Locate and identify every blood parasite.
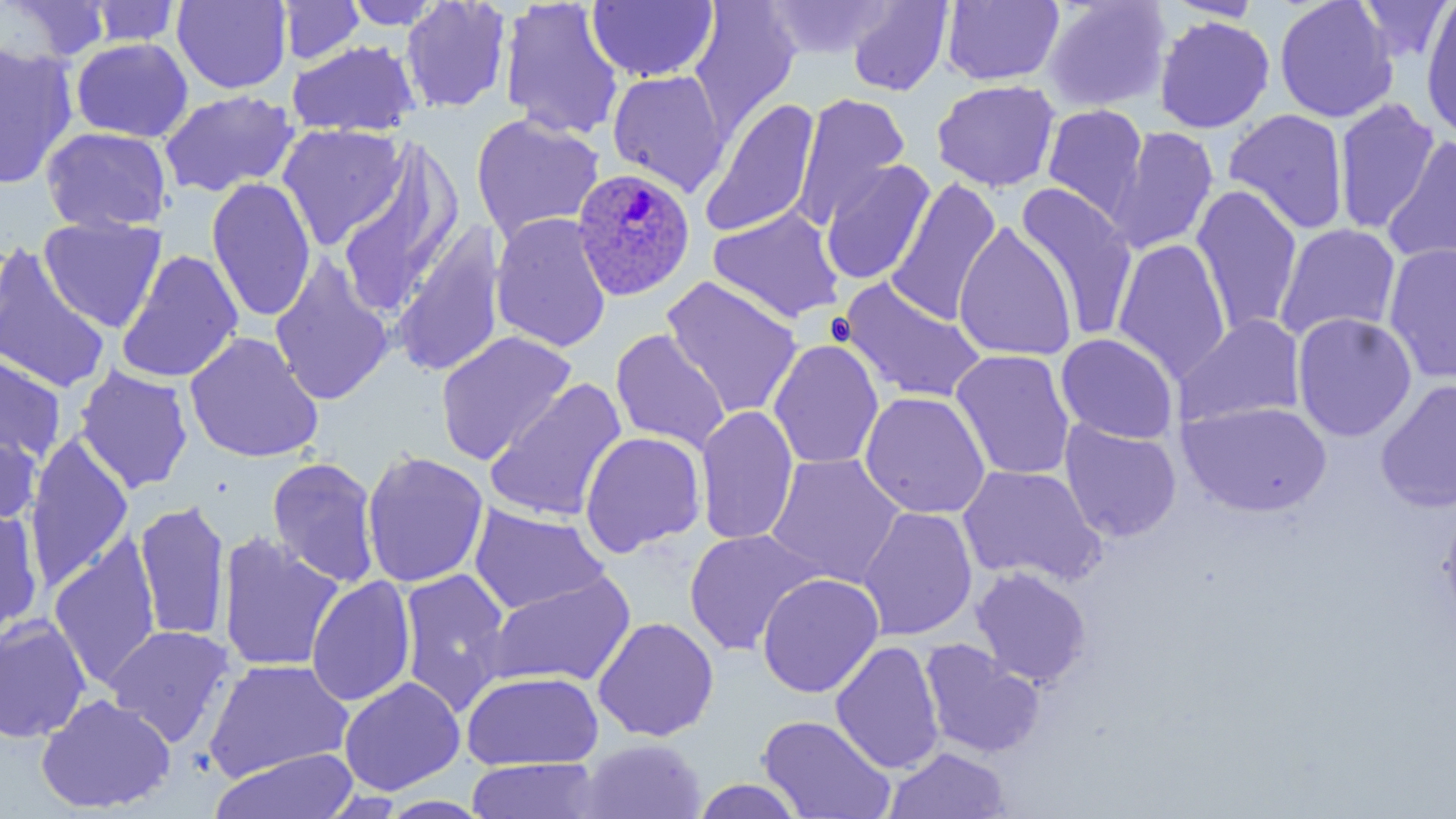

Approximate bounding boxes as [x1, y1, x2, y2] in pixels.
Plasmodium ovale-infected red blood cells: [572, 167, 695, 302].
No Plasmodium falciparum, Plasmodium malariae, Plasmodium vivax, Babesia divergens, or Trypanosoma brucei observed.

slide-level diagnosis = Plasmodium ovale
uninfected red blood cell locations = approximate bounding boxes as [x1, y1, x2, y2] in pixels: [2, 0, 112, 63], [498, 0, 624, 140], [586, 0, 719, 83], [941, 0, 1064, 86], [1041, 0, 1173, 113], [1355, 0, 1453, 62], [84, 1, 183, 47], [171, 1, 292, 94], [277, 1, 366, 65], [340, 1, 446, 30], [400, 1, 512, 114], [688, 1, 801, 137], [760, 1, 896, 61], [846, 1, 952, 96], [1273, 1, 1399, 123], [1420, 1, 1456, 141], [1152, 15, 1275, 135], [71, 38, 193, 142], [286, 39, 420, 137], [0, 43, 78, 188], [607, 69, 729, 196], [931, 79, 1060, 192], [159, 89, 299, 198], [793, 93, 910, 226], [700, 98, 820, 239], [1332, 98, 1440, 234], [1040, 103, 1150, 222], [1223, 108, 1350, 235], [469, 113, 605, 244], [277, 123, 407, 249], [1108, 125, 1218, 254], [41, 126, 172, 234], [1383, 137, 1456, 266], [337, 142, 462, 314], [820, 160, 935, 285], [206, 177, 315, 322], [886, 177, 1002, 326], [1015, 182, 1139, 341], [1191, 184, 1302, 337], [707, 207, 845, 324], [490, 213, 612, 353], [38, 216, 166, 332], [953, 222, 1077, 362], [391, 223, 506, 379], [1274, 223, 1401, 343], [1112, 239, 1231, 383], [1383, 243, 1456, 384], [0, 246, 112, 394], [116, 250, 244, 384], [269, 259, 395, 407], [661, 276, 803, 419], [839, 279, 987, 403], [1291, 312, 1417, 442], [1175, 314, 1305, 430], [610, 329, 730, 452], [184, 331, 323, 463], [436, 331, 577, 465], [1055, 333, 1178, 443], [768, 339, 884, 470], [950, 349, 1076, 481], [0, 353, 66, 464], [73, 365, 193, 494], [484, 378, 628, 522], [1376, 379, 1456, 514], [859, 390, 991, 519], [1178, 401, 1331, 517], [695, 406, 798, 546], [1059, 420, 1182, 543], [0, 429, 41, 527], [579, 430, 705, 557], [24, 434, 134, 591], [361, 450, 488, 588], [765, 452, 905, 587], [267, 456, 381, 587], [957, 465, 1106, 585], [133, 500, 231, 642], [1438, 503, 1456, 627], [469, 505, 609, 615], [858, 506, 978, 641], [0, 507, 43, 636], [683, 528, 824, 655], [216, 533, 344, 673], [49, 536, 161, 690], [970, 567, 1091, 687], [397, 568, 512, 713], [484, 571, 636, 688], [756, 572, 884, 698], [306, 575, 416, 707], [0, 614, 92, 743], [592, 616, 719, 742], [104, 624, 234, 746], [919, 638, 1044, 759], [830, 640, 945, 774], [204, 658, 354, 783], [461, 671, 603, 770], [339, 676, 465, 795], [36, 693, 176, 814], [756, 714, 896, 818], [579, 738, 706, 819], [884, 746, 1011, 819], [209, 748, 360, 819], [464, 757, 604, 818], [690, 778, 807, 818]
modality = optical microscopy
magnification = 1000x
preparation = thin blood smear
field of view = one of a larger specimen
stain = May-Grünwald-Giemsa
platelet locations = approximate bounding boxes as [x1, y1, x2, y2] in pixels: [828, 314, 855, 347]
image size = 1456×819 pixels